Give the position of every Plasmodium falciparum parasite, noting its life-cycle stage.
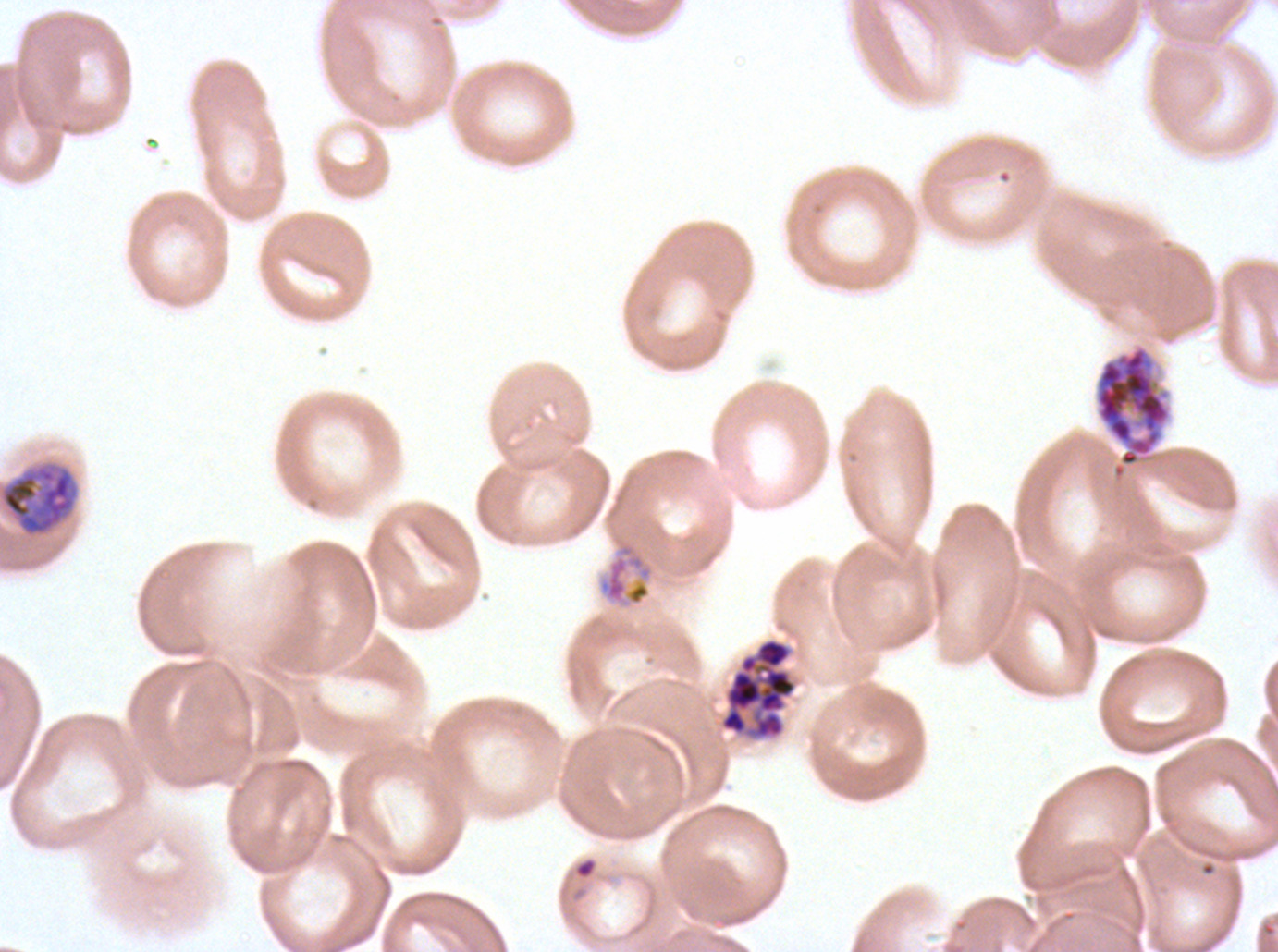

Approximate bounding boxes as [x1, y1, x2, y2] in pixels.
Rings: [574, 857, 597, 879].
Late trophozoites: [0, 465, 75, 535].
Early schizonts: [1095, 347, 1170, 467], [597, 542, 654, 606].
Segmenters: [719, 637, 797, 740].
No late-ring/early-trophozoite forms, mid trophozoites, late schizonts, or gametocytes observed.

Giemsa stain. Life-cycle stages observed: ring, late trophozoite, early schizont, segmenter. Plasmodium falciparum cultured ex vivo for 24 to 48 hours, from a patient in The Gambia. A sub-image separated from a larger composite. Thin blood smear. Image is 1278×952 pixels.